Name the parasite shown.
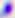

This is Toxoplasma gondii.

modality = micrograph
magnification = 400x